Report the malaria status of this cell.
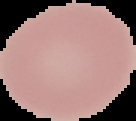

Uninfected.

From a thin blood film. Image is 136×121 pixels. Cell region segmented out of the field of view; the surrounding area is masked to black.